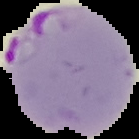
From a thin blood smear. Malaria status: parasitized. Image is 139×139 pixels. Cell region segmented out of the field of view; the surrounding area is masked to black.